Classify this cell by malaria status.
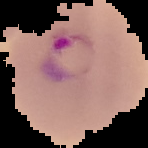

Parasitized.

The area outside the segmented cell region is set to black. Image is 148×148 pixels. From a thin blood film.